Locate and identify every blood parasite.
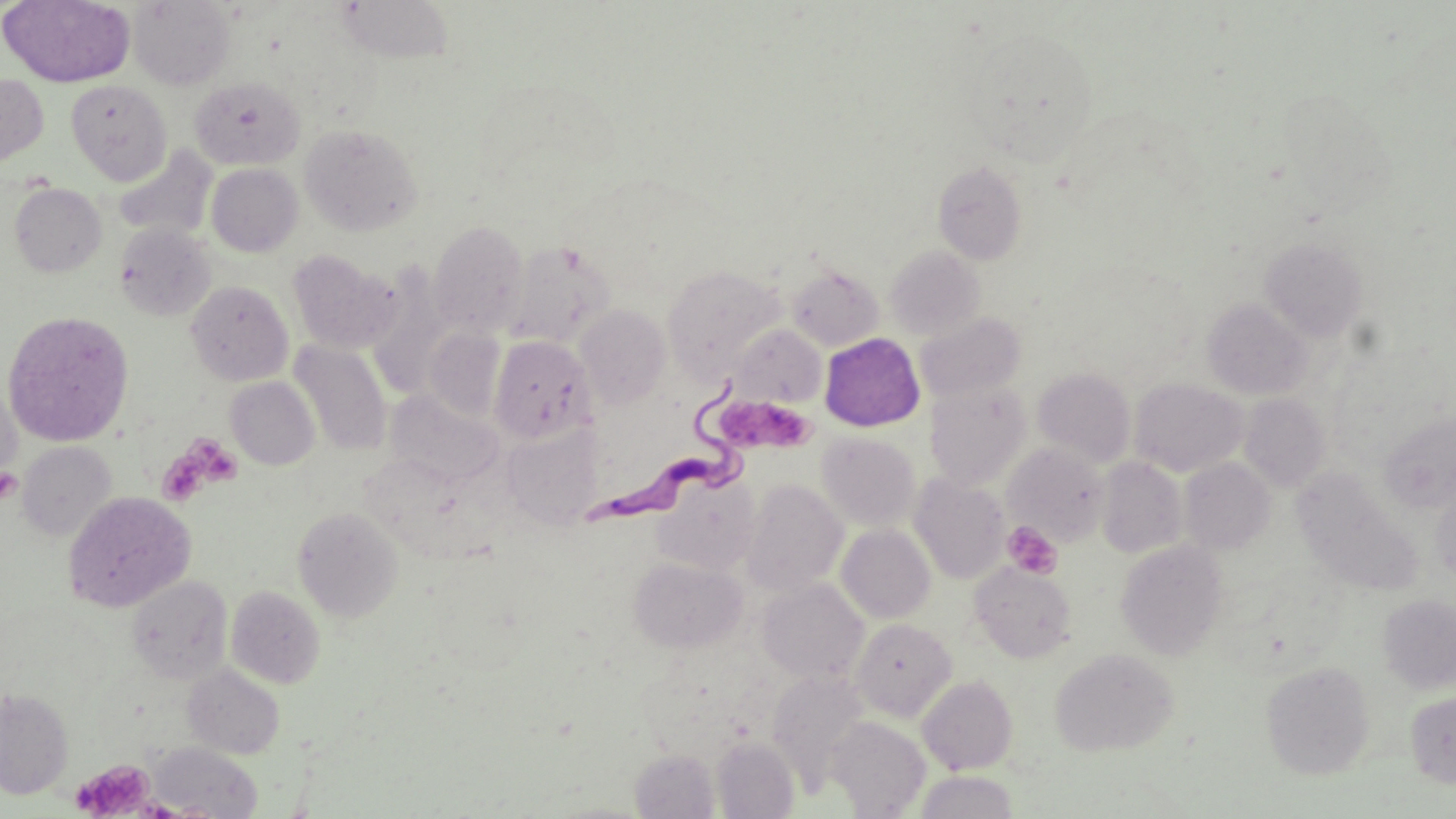
Approximate bounding boxes as named x1/y1/x2/y2 corners in pixels.
Trypanosoma brucei: (x1=589, y1=369, x2=751, y2=528).
No Plasmodium falciparum, Plasmodium ovale, Plasmodium malariae, Plasmodium vivax, or Babesia divergens observed.

Summary:
  - Platelet locations: (x1=720, y1=404, x2=815, y2=450), (x1=161, y1=434, x2=244, y2=503), (x1=0, y1=468, x2=22, y2=504), (x1=1003, y1=521, x2=1061, y2=578), (x1=72, y1=759, x2=156, y2=819)
  - Uninfected red blood cell locations: (x1=1, y1=0, x2=136, y2=88), (x1=129, y1=1, x2=235, y2=89), (x1=335, y1=1, x2=455, y2=64), (x1=963, y1=26, x2=1100, y2=162), (x1=0, y1=73, x2=49, y2=167), (x1=189, y1=76, x2=305, y2=169), (x1=65, y1=80, x2=171, y2=184), (x1=299, y1=123, x2=424, y2=236), (x1=115, y1=146, x2=217, y2=241), (x1=933, y1=161, x2=1028, y2=265), (x1=205, y1=163, x2=303, y2=256), (x1=9, y1=183, x2=107, y2=278), (x1=429, y1=221, x2=529, y2=334), (x1=114, y1=222, x2=216, y2=321), (x1=1260, y1=237, x2=1369, y2=341), (x1=504, y1=240, x2=616, y2=348), (x1=884, y1=245, x2=985, y2=340), (x1=287, y1=250, x2=400, y2=354), (x1=787, y1=264, x2=884, y2=351), (x1=662, y1=265, x2=784, y2=379), (x1=185, y1=280, x2=294, y2=386), (x1=1202, y1=298, x2=1313, y2=399), (x1=576, y1=304, x2=671, y2=409), (x1=1, y1=310, x2=135, y2=447), (x1=915, y1=311, x2=1025, y2=402), (x1=731, y1=324, x2=826, y2=407), (x1=424, y1=327, x2=506, y2=422), (x1=819, y1=333, x2=925, y2=431), (x1=488, y1=335, x2=594, y2=443), (x1=290, y1=342, x2=392, y2=455), (x1=1033, y1=367, x2=1135, y2=467), (x1=225, y1=377, x2=320, y2=470), (x1=1129, y1=378, x2=1246, y2=477), (x1=0, y1=379, x2=22, y2=485), (x1=925, y1=383, x2=1031, y2=489), (x1=385, y1=388, x2=504, y2=488), (x1=1238, y1=393, x2=1331, y2=492), (x1=1379, y1=413, x2=1456, y2=514), (x1=501, y1=425, x2=603, y2=531), (x1=817, y1=433, x2=921, y2=531), (x1=16, y1=441, x2=118, y2=541), (x1=1003, y1=443, x2=1110, y2=545), (x1=1096, y1=457, x2=1188, y2=558), (x1=1180, y1=457, x2=1275, y2=553), (x1=1291, y1=468, x2=1422, y2=594), (x1=653, y1=473, x2=761, y2=575), (x1=909, y1=473, x2=1010, y2=584), (x1=741, y1=479, x2=848, y2=595), (x1=1430, y1=484, x2=1456, y2=586), (x1=62, y1=491, x2=195, y2=612), (x1=293, y1=506, x2=403, y2=622), (x1=836, y1=524, x2=935, y2=623), (x1=1116, y1=540, x2=1229, y2=660), (x1=629, y1=555, x2=747, y2=652), (x1=971, y1=562, x2=1077, y2=663), (x1=126, y1=575, x2=233, y2=684), (x1=757, y1=578, x2=869, y2=684), (x1=226, y1=585, x2=325, y2=688), (x1=1377, y1=594, x2=1456, y2=693), (x1=850, y1=619, x2=956, y2=721), (x1=1050, y1=648, x2=1178, y2=757), (x1=1261, y1=660, x2=1375, y2=779), (x1=183, y1=665, x2=285, y2=759), (x1=767, y1=670, x2=870, y2=790), (x1=917, y1=675, x2=1018, y2=774), (x1=0, y1=689, x2=74, y2=799), (x1=1405, y1=691, x2=1456, y2=788), (x1=828, y1=716, x2=930, y2=817), (x1=712, y1=736, x2=799, y2=818), (x1=147, y1=742, x2=262, y2=817), (x1=630, y1=749, x2=719, y2=818), (x1=914, y1=770, x2=1019, y2=818)
  - Slide-level diagnosis: Trypanosoma brucei
  - Preparation: thin blood film
  - Image size: 1456×819 pixels
  - Modality: light microscopy
  - Stain: May-Grünwald-Giemsa
  - Magnification: 1000x
  - Field of view: single